Identify the preparation type.
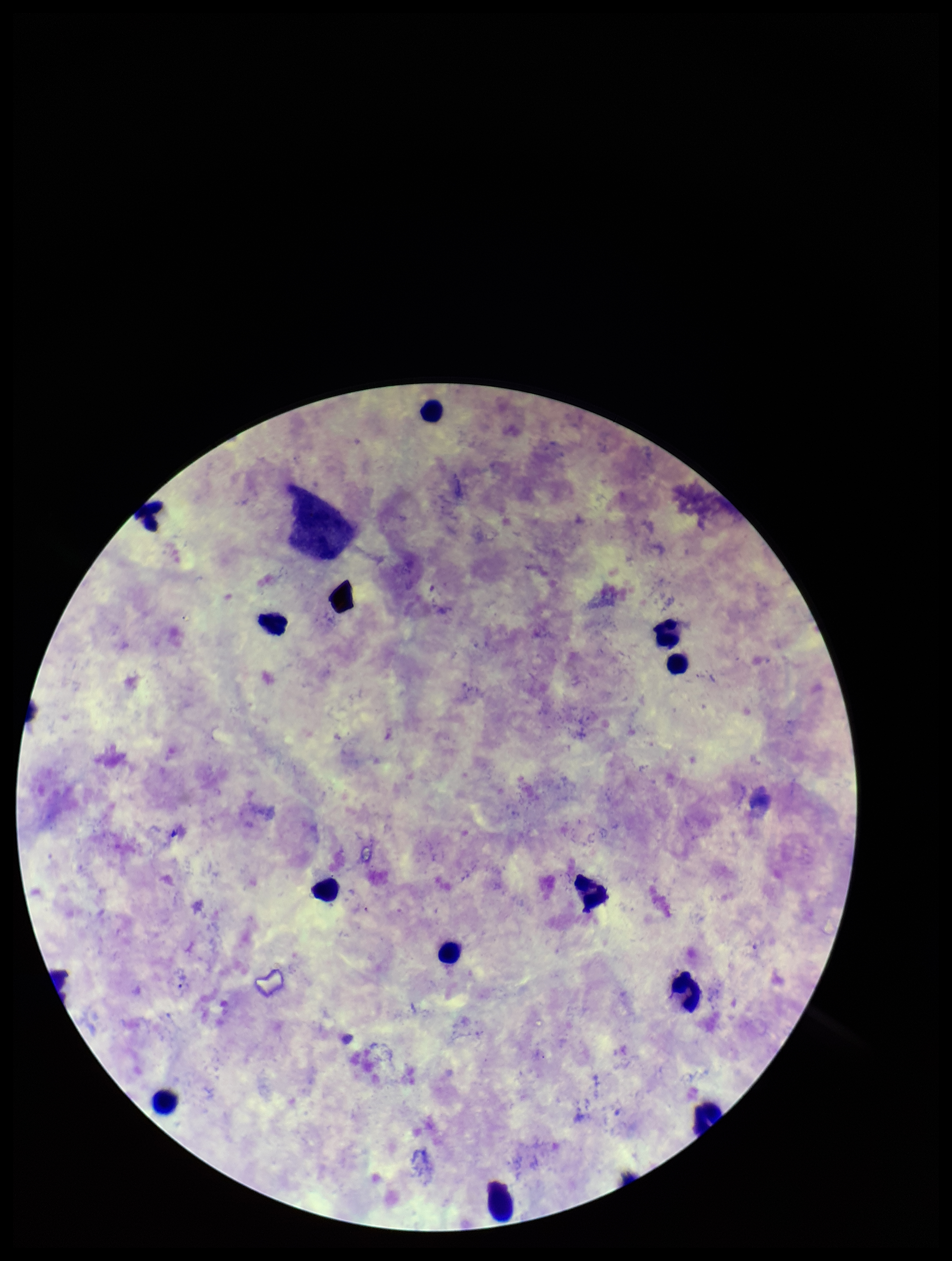

Thick.

Summary:
  - Field of view: single
  - Parasite count: 1
  - Patient malaria status: infected
  - Leukocyte count: 12
  - Species reported for this patient: Plasmodium vivax
  - Stain: Giemsa
  - Plasmodium parasites: seen
  - Capture: smartphone photograph through the microscope eyepiece
  - Image size: 952×1261 pixels